Point out each Plasmodium parasite.
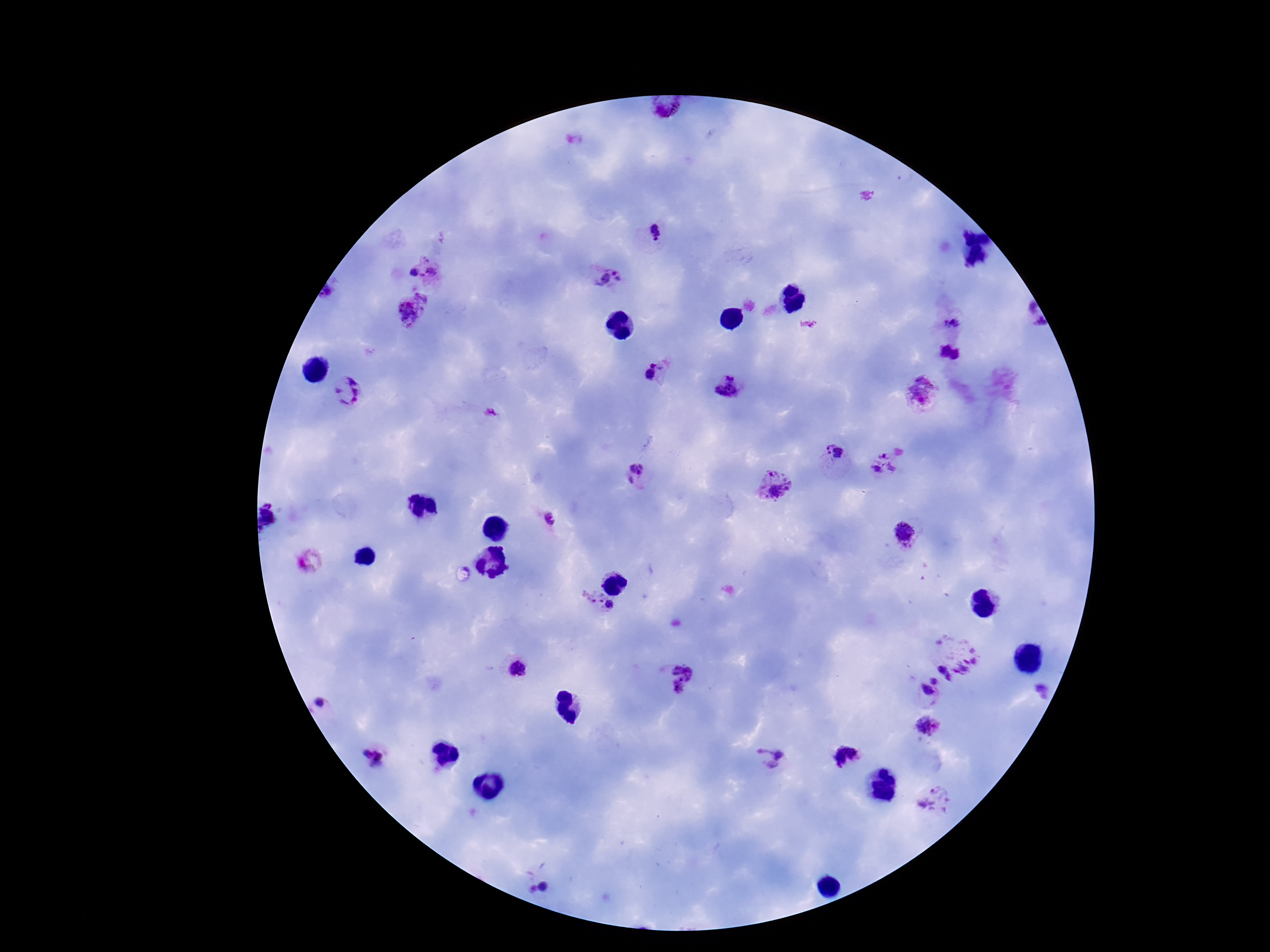

Approximate object centers, in pixels from the top-left corner.
Plasmodium parasites: (x=668, y=108), (x=655, y=232), (x=426, y=270), (x=604, y=275), (x=413, y=311), (x=951, y=323), (x=949, y=355), (x=659, y=372), (x=729, y=386), (x=351, y=391), (x=921, y=393), (x=832, y=456), (x=884, y=464), (x=635, y=475), (x=772, y=487), (x=552, y=521), (x=906, y=533), (x=595, y=599), (x=611, y=608), (x=963, y=654), (x=518, y=668), (x=947, y=672), (x=682, y=678), (x=936, y=678), (x=1043, y=690), (x=929, y=692), (x=326, y=705), (x=929, y=726), (x=776, y=755), (x=844, y=756), (x=376, y=758), (x=937, y=802).

Single field of view. 100x magnification. Giemsa stain. Thick blood film. Smartphone photograph taken through the microscope eyepiece. Patient malaria status: positive. Image is 1270×952 pixels.